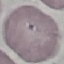
result = no malaria parasites detected
preparation = thin smear
capture = smartphone camera at the microscope eyepiece
stain = Giemsa
image type = cell patch, automatically extracted from a larger field of view and resized to 64 × 64 pixels